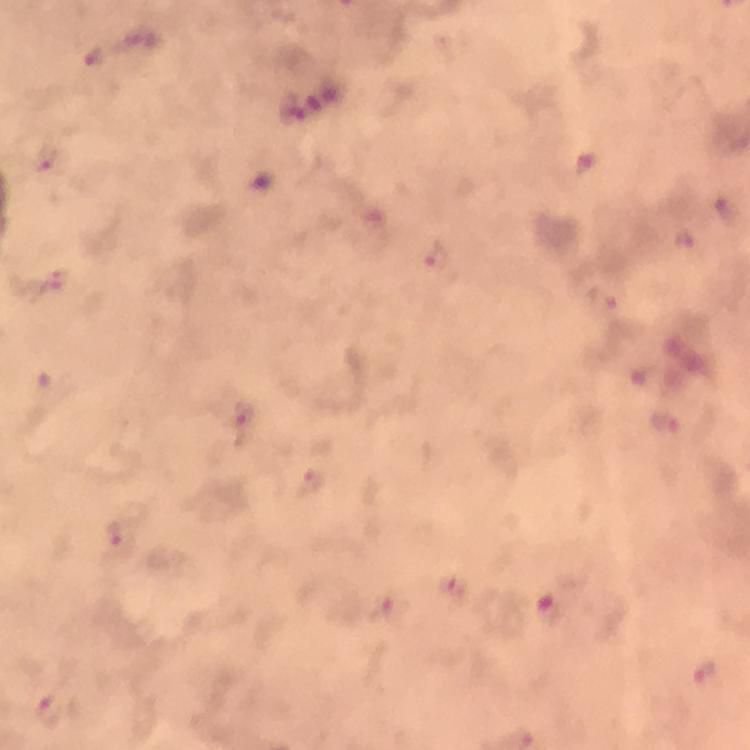
magnification = 100x
image size = 750×750 pixels
context = from a diagnostic examination for malaria
Plasmodium parasite locations = approximate centers as [x, y] in pixels: [96, 58], [300, 111], [45, 158], [263, 182], [439, 256], [666, 422], [311, 481], [121, 534], [386, 607], [549, 609], [706, 672], [49, 708]
immersion oil = applied
capture = smartphone photograph through a microscope
preparation = thick blood film
stain = Giemsa
cropped from = a single field of view